Give the position of every leukocyte visible.
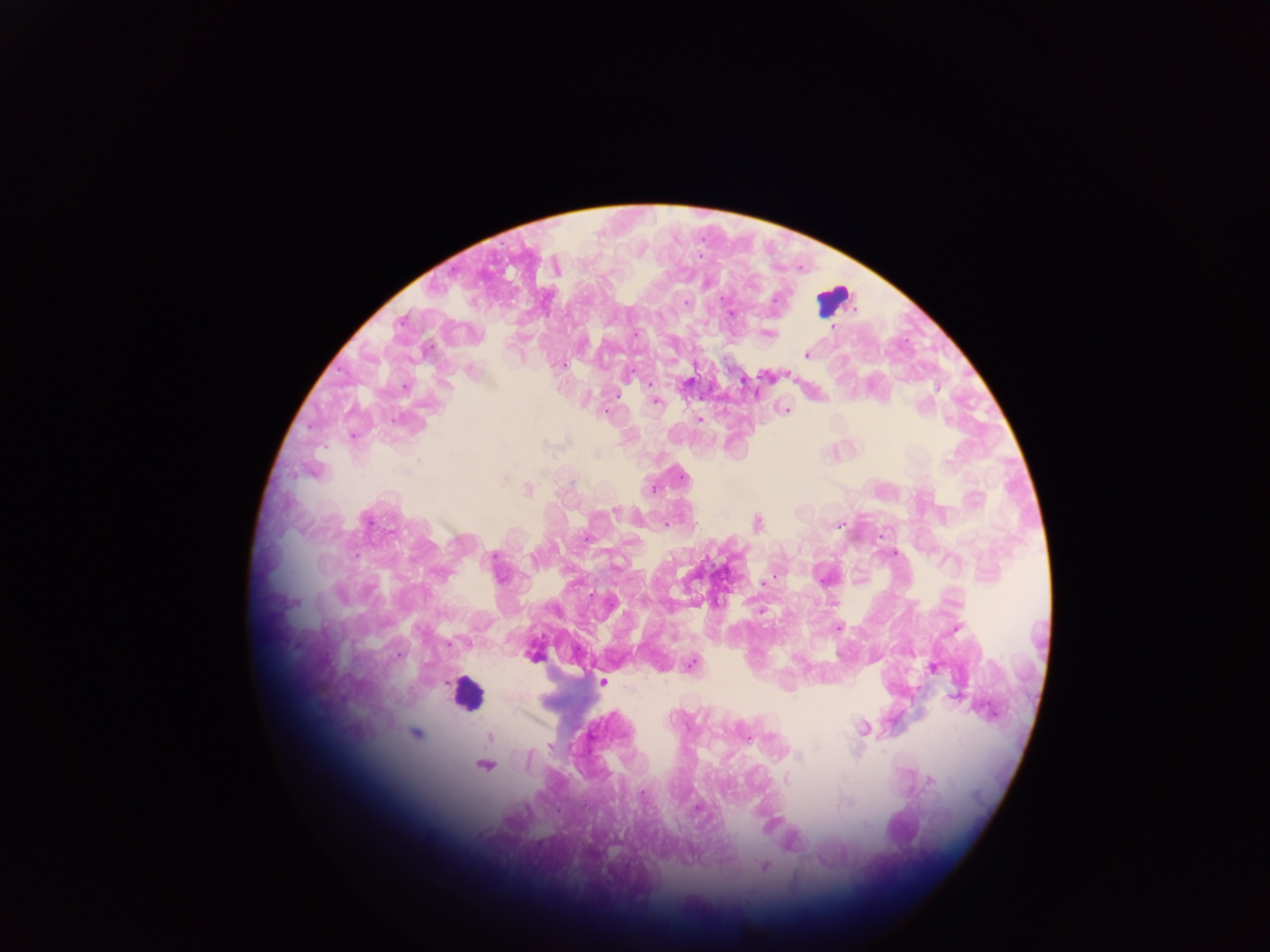

Approximate centers as (x, y) in pixels.
Leukocytes: (834, 299), (466, 692).

Plasmodium parasite locations: (722, 299), (685, 302), (731, 314), (833, 327), (769, 333), (635, 334), (807, 355), (563, 365), (630, 372), (689, 381), (650, 384), (405, 387), (937, 388), (655, 401), (922, 407), (785, 410), (606, 412), (700, 419), (949, 420), (948, 460), (682, 476), (653, 488), (527, 489), (616, 511), (665, 524), (758, 524), (839, 525), (588, 538), (894, 553), (494, 557), (774, 575), (761, 611), (838, 627), (955, 630), (533, 655), (691, 665), (933, 668), (602, 682), (863, 728), (415, 733), (747, 737), (490, 738), (551, 747), (799, 757), (483, 765), (786, 781), (930, 781), (642, 792), (697, 808), (867, 826), (765, 866). One field of view. Image is 1270×952 pixels. Mobile-phone photograph taken through the microscope. Sample from Ghana. Thick blood smear.